Locate every malaria parasite.
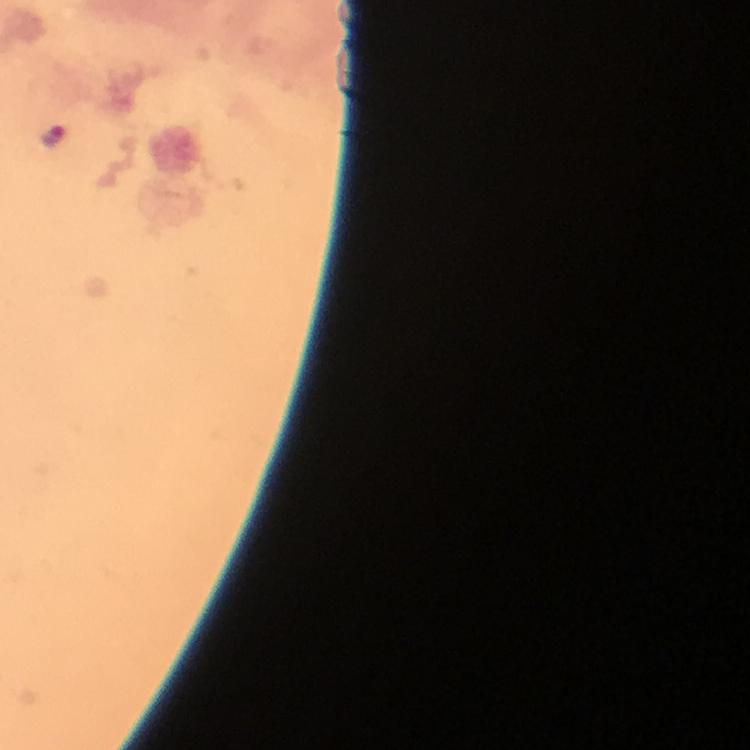

Approximate centers as {x, y} in pixels.
Malaria parasites: {54, 136}.

Summary:
  - Immersion oil: applied
  - Magnification: 100x
  - Preparation: thick blood film
  - Image size: 750×750 pixels
  - Cropped from: one field of view
  - Context: from a diagnostic examination for malaria
  - Capture: smartphone mounted on the microscope
  - Stain: Giemsa